Locate and identify every blood parasite.
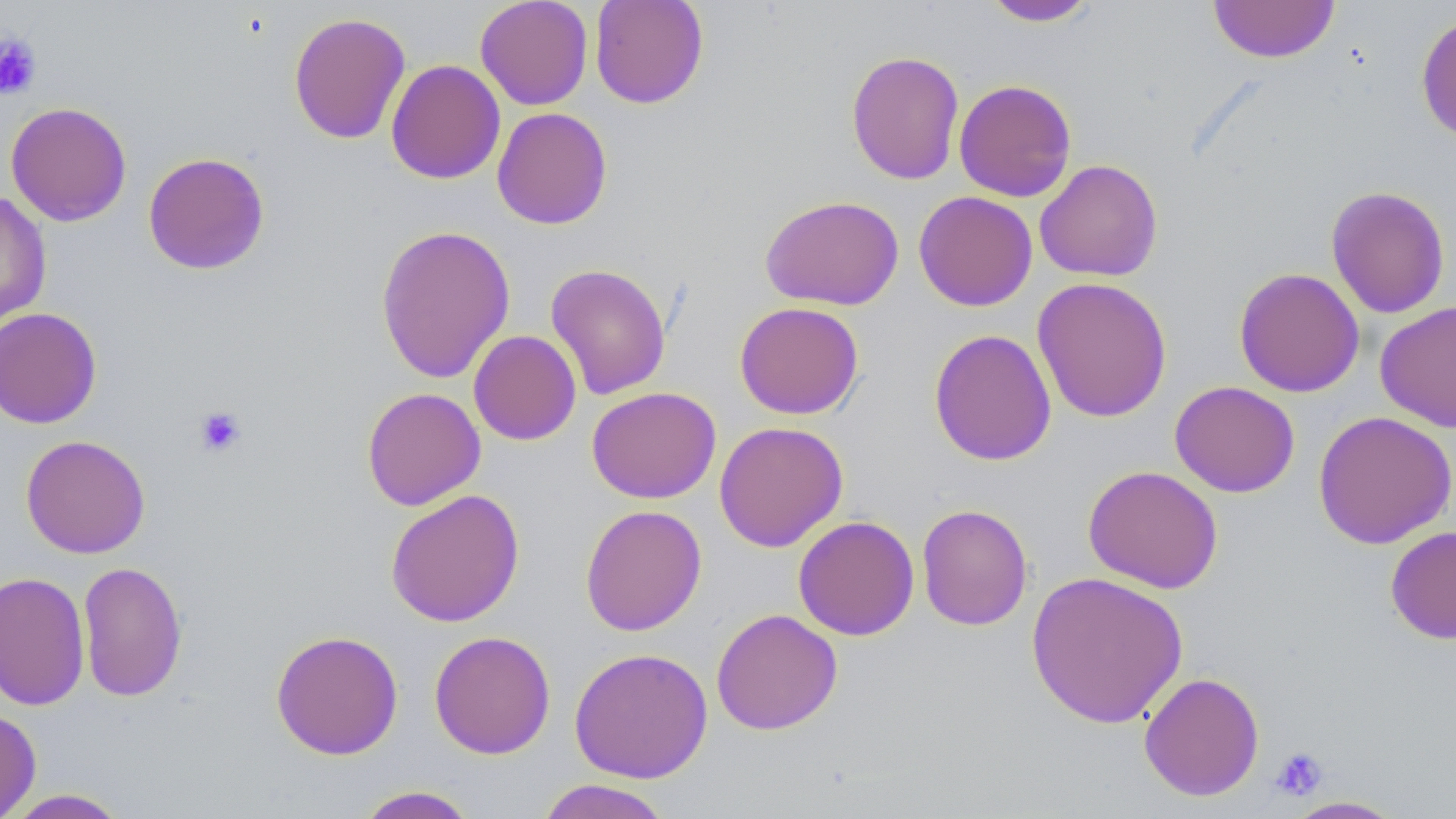
No blood parasites seen.

Summary:
  - Coordinate format: approximate bounding boxes as [x1, y1, x2, y2] in pixels
  - Platelet locations: [0, 32, 42, 99], [193, 405, 247, 457], [1270, 746, 1330, 801]
  - Uninfected red blood cell locations: [475, 0, 593, 110], [590, 0, 709, 109], [980, 0, 1099, 27], [1208, 1, 1340, 64], [1416, 11, 1456, 145], [288, 12, 411, 145], [845, 49, 965, 185], [385, 59, 506, 185], [953, 79, 1077, 202], [5, 101, 132, 226], [491, 107, 613, 230], [143, 151, 270, 275], [1034, 159, 1163, 282], [1325, 185, 1451, 319], [0, 191, 52, 330], [913, 191, 1038, 311], [760, 194, 904, 310], [375, 223, 516, 383], [545, 263, 671, 400], [1233, 267, 1365, 397], [1032, 276, 1172, 423], [1375, 300, 1456, 433], [734, 301, 864, 419], [0, 307, 102, 429], [928, 328, 1057, 466], [468, 329, 582, 445], [1169, 381, 1300, 497], [586, 386, 721, 503], [361, 387, 486, 511], [1312, 410, 1456, 549], [713, 421, 849, 552], [20, 434, 151, 559], [1083, 465, 1224, 593], [385, 489, 525, 627], [916, 503, 1033, 631], [579, 504, 707, 636], [793, 515, 920, 641], [1385, 526, 1456, 645], [77, 560, 188, 703], [0, 571, 90, 711], [1025, 571, 1189, 729], [711, 608, 843, 735], [270, 629, 403, 760], [429, 630, 556, 759], [569, 647, 713, 783], [1138, 671, 1265, 801], [0, 708, 41, 818], [534, 779, 675, 819], [355, 785, 479, 818], [3, 788, 132, 818], [1280, 796, 1409, 818]
  - Slide-level diagnosis: negative for blood parasites
  - Stain: May-Grünwald-Giemsa
  - Field of view: single
  - Preparation: thin blood smear
  - Modality: optical microscopy
  - Image size: 1456×819 pixels
  - Magnification: 1000x